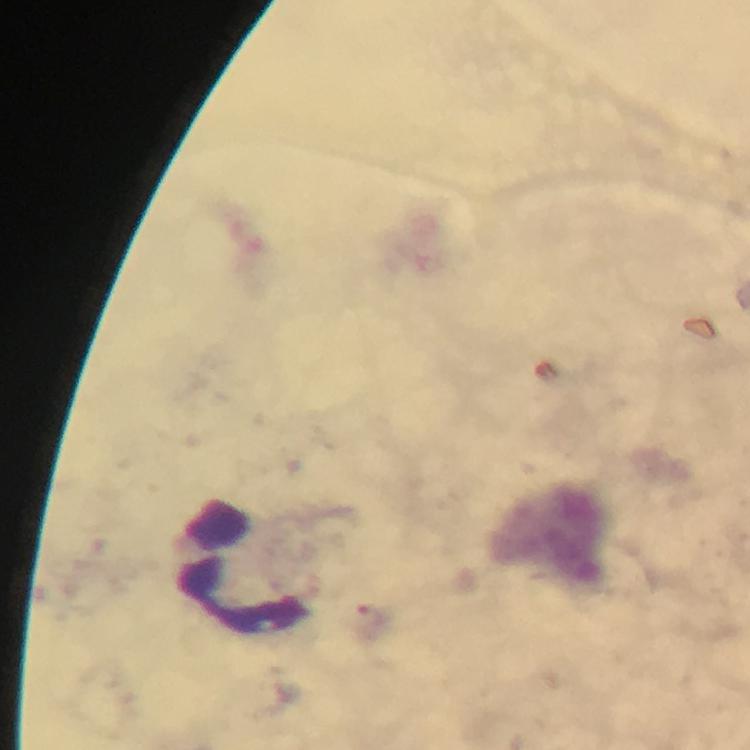
Approximate centers as {x, y} in pixels.
Summary:
  - Leukocyte locations: {240, 565}
  - Plasmodium parasite locations: {372, 622}
  - Capture: smartphone camera through the microscope
  - Stain: Giemsa
  - Context: from a malaria diagnostic workup
  - Magnification: 100x
  - Cropped from: one field of view
  - Image size: 750×750 pixels
  - Preparation: thick blood film
  - Immersion oil: used